Give the preparation type.
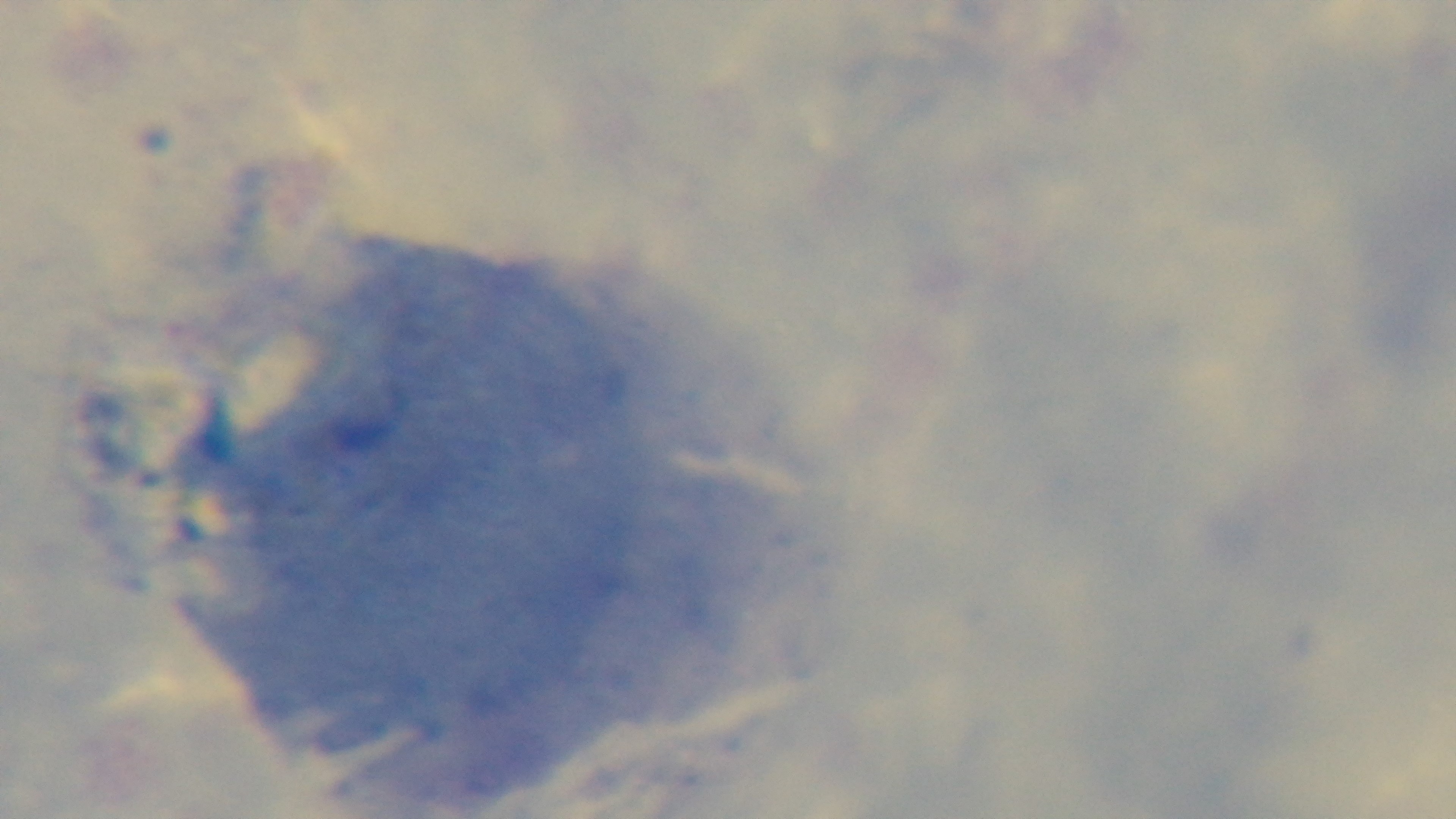
A thick smear.

100x oil-immersion objective. Malaria status: negative. One field from the slide. Giemsa-stained. Photomicrograph. Mounted 4K digital camera.